Locate every Plasmodium parasite.
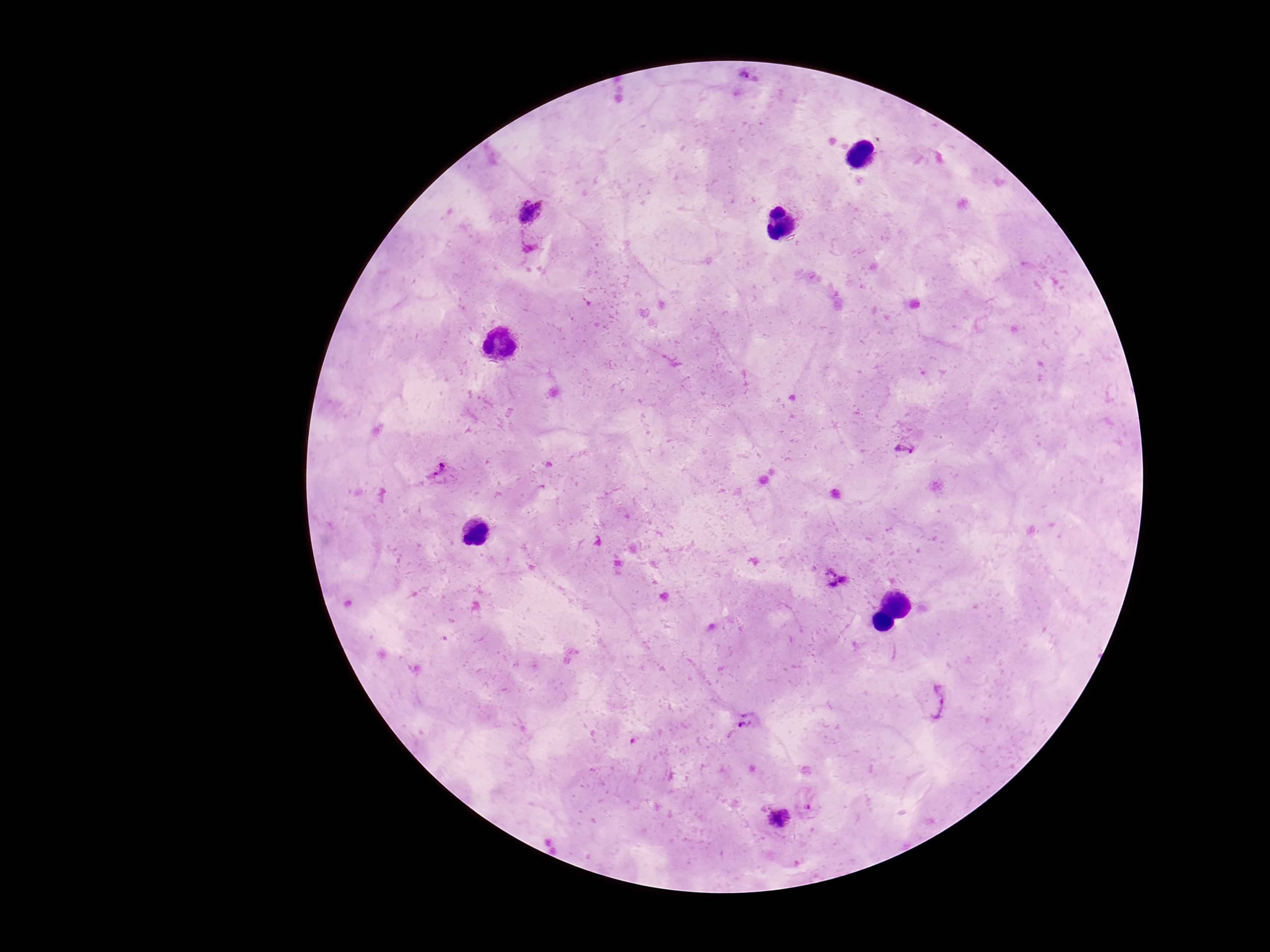
Approximate object centers, in pixels from the top-left corner.
Plasmodium parasites: (x=749, y=74), (x=531, y=211), (x=904, y=448), (x=440, y=471), (x=836, y=578), (x=942, y=701), (x=747, y=721), (x=812, y=802), (x=778, y=819).

{
  "field_of_view": "single",
  "image_size": "1270×952 pixels",
  "stain": "Giemsa",
  "magnification": "100x",
  "patient_malaria_status": "positive",
  "capture": "smartphone camera through the microscope eyepiece",
  "preparation": "thick blood film"
}